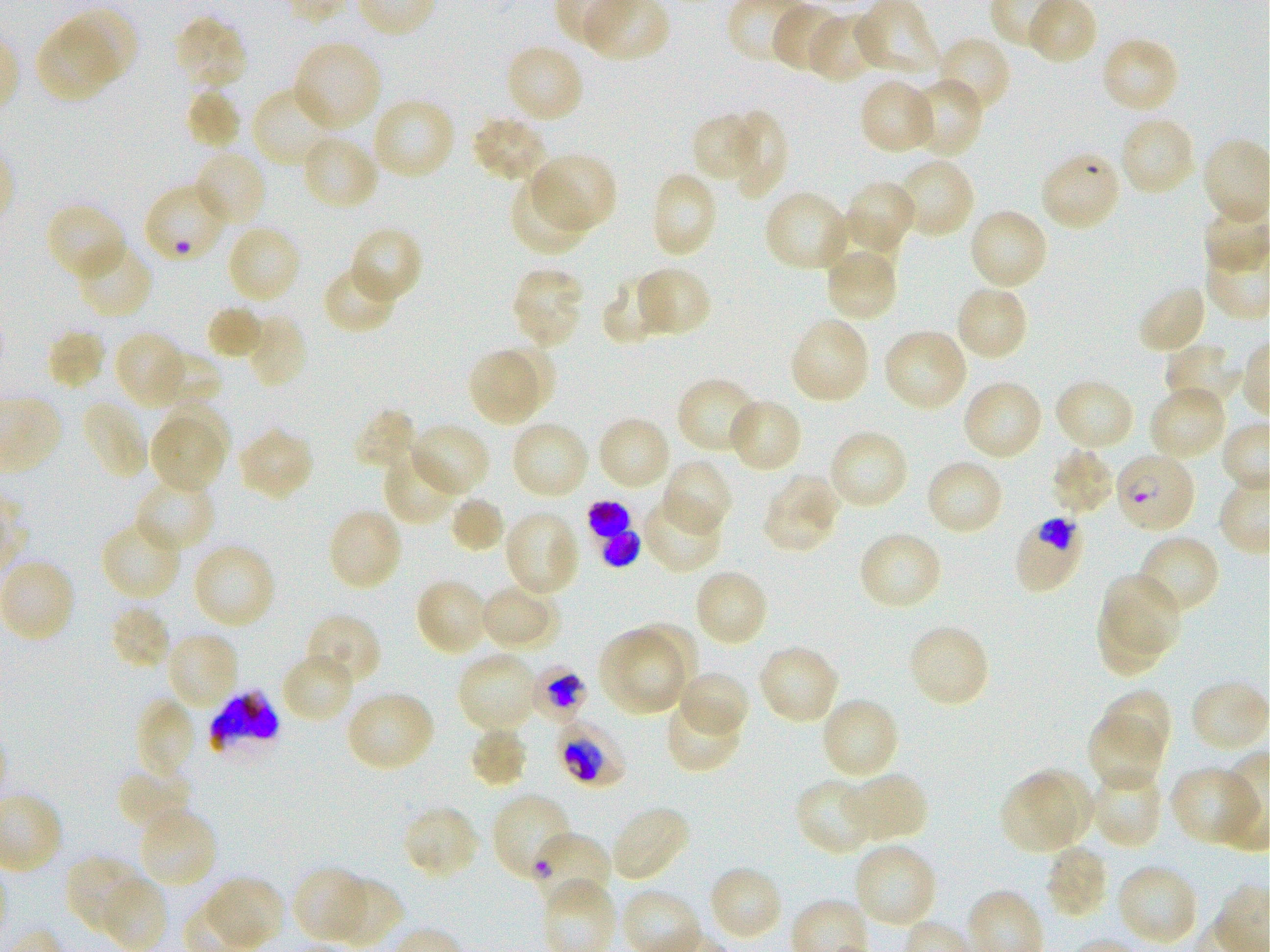
Not every red blood cell is marked. A life-cycle stage — or a range of stages, where the recorded stages span more than one — follows each staged infected red blood cell.
{
  "stain": "Giemsa",
  "life_cycle_stages_observed": "ring, trophozoite",
  "objective": "100x, oil immersion, numerical aperture 1.25",
  "image_size": "1270×952 pixels",
  "field_of_view": "one from this slide",
  "donor_blood_group": "O+",
  "locations_of_uninfected_red_blood_cells": "approximate bounding boxes as (x1, y1, x2, y2) in pixels: (855, 0, 939, 79), (770, 4, 844, 74), (58, 8, 140, 85), (807, 12, 877, 83), (171, 14, 248, 92), (34, 24, 117, 104), (935, 35, 1012, 116), (1100, 35, 1181, 115), (293, 40, 382, 132), (505, 44, 585, 124), (904, 77, 985, 159), (858, 78, 936, 156), (253, 84, 340, 167), (185, 87, 242, 150), (371, 96, 456, 182), (691, 111, 759, 187), (728, 111, 788, 200), (469, 115, 549, 185), (1118, 116, 1197, 197), (300, 135, 380, 211), (193, 149, 269, 229), (531, 153, 617, 234), (896, 157, 976, 239), (648, 169, 718, 260), (509, 177, 589, 257), (843, 180, 918, 255), (764, 190, 852, 274), (44, 202, 127, 282), (967, 207, 1049, 292), (822, 212, 899, 287), (225, 223, 302, 305), (349, 227, 422, 304), (75, 241, 155, 319), (824, 249, 900, 322), (322, 263, 399, 334), (634, 265, 712, 339), (511, 267, 585, 349), (601, 274, 669, 347), (1135, 283, 1208, 357), (953, 285, 1029, 362), (205, 304, 265, 361), (246, 313, 309, 389), (788, 316, 872, 405), (46, 327, 104, 391), (882, 328, 969, 412), (114, 331, 187, 408), (1163, 343, 1244, 409), (495, 344, 558, 408), (148, 348, 218, 410), (471, 351, 537, 425), (677, 375, 760, 454), (1053, 378, 1136, 452), (962, 380, 1044, 461), (1148, 384, 1228, 461), (726, 396, 804, 474), (80, 398, 148, 480), (165, 398, 233, 470), (351, 407, 420, 474), (597, 415, 672, 491), (510, 420, 590, 500), (149, 421, 223, 493), (409, 422, 491, 499), (236, 427, 315, 502), (828, 428, 910, 511), (1049, 447, 1116, 518), (382, 450, 461, 525), (661, 458, 734, 538), (925, 458, 1004, 537), (761, 474, 840, 554), (133, 477, 217, 554), (449, 495, 506, 555), (641, 497, 725, 574), (326, 507, 404, 593), (503, 509, 581, 595), (99, 519, 183, 602), (856, 531, 944, 612), (1136, 534, 1222, 618), (192, 542, 277, 629), (0, 559, 76, 643), (692, 568, 770, 648), (1101, 573, 1181, 655), (415, 577, 489, 657), (481, 584, 560, 650), (1096, 601, 1169, 678), (109, 604, 172, 671), (304, 612, 384, 689), (622, 622, 699, 700), (906, 622, 991, 709), (599, 627, 684, 716), (165, 630, 240, 712), (757, 643, 841, 725), (457, 650, 538, 733), (281, 651, 356, 724), (677, 669, 750, 737), (1191, 681, 1268, 754), (1100, 689, 1172, 758), (345, 690, 436, 773), (664, 694, 743, 773), (819, 696, 900, 781), (134, 697, 196, 780), (1088, 712, 1165, 792), (467, 725, 529, 789), (116, 765, 193, 834), (1171, 765, 1261, 848), (1025, 767, 1096, 841), (1089, 768, 1164, 850), (840, 771, 930, 841), (1001, 776, 1075, 855), (796, 780, 872, 855), (400, 804, 482, 881), (609, 804, 690, 884), (138, 807, 219, 889), (853, 841, 938, 928), (1043, 844, 1111, 921), (63, 854, 141, 935), (1115, 862, 1200, 947), (707, 865, 784, 943), (290, 867, 370, 944), (100, 874, 168, 950), (326, 875, 403, 947), (201, 877, 284, 949)",
  "locations_of_infected_red_blood_cells": "approximate bounding boxes as (x1, y1, x2, y2) in pixels: (1114, 451, 1197, 534) ring; (585, 500, 640, 566); (1013, 515, 1087, 595); (529, 666, 589, 724) trophozoite; (208, 691, 282, 754); (551, 714, 627, 789) trophozoite; (531, 833, 612, 912) early ring to early trophozoite",
  "locations_of_red_blood_cells_of_indeterminate_infection_status": "approximate bounding boxes as (x1, y1, x2, y2) in pixels: (1039, 151, 1123, 234), (490, 792, 574, 881)",
  "culture": "in-vitro Plasmodium falciparum strain 3D7, static",
  "preparation": "thin blood smear"
}